Name the parasite shown.
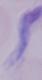

This is a trypanosome.

modality: photomicrograph
magnification: 1000x